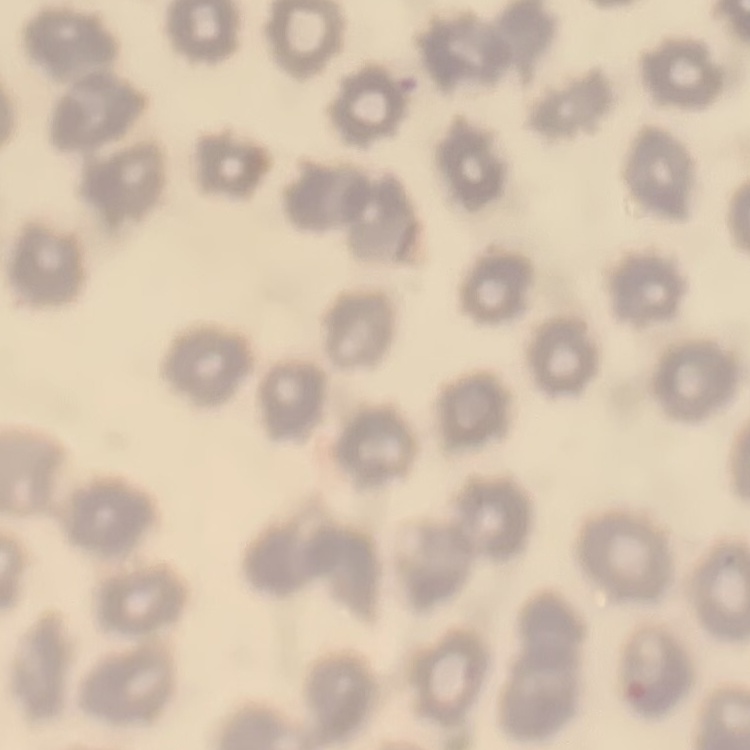
Summary:
  - Red blood cell morphology: no rouleaux formation
  - Stain: Field's or Giemsa
  - Preparation: thin blood smear
  - Image type: one tile cut from a larger photomicrograph